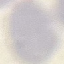

malaria status = uninfected
image type = cell patch, automatically extracted from a larger field of view and resized to 64 × 64 pixels
capture = smartphone camera at the microscope eyepiece
preparation = thin blood film
stain = Giemsa